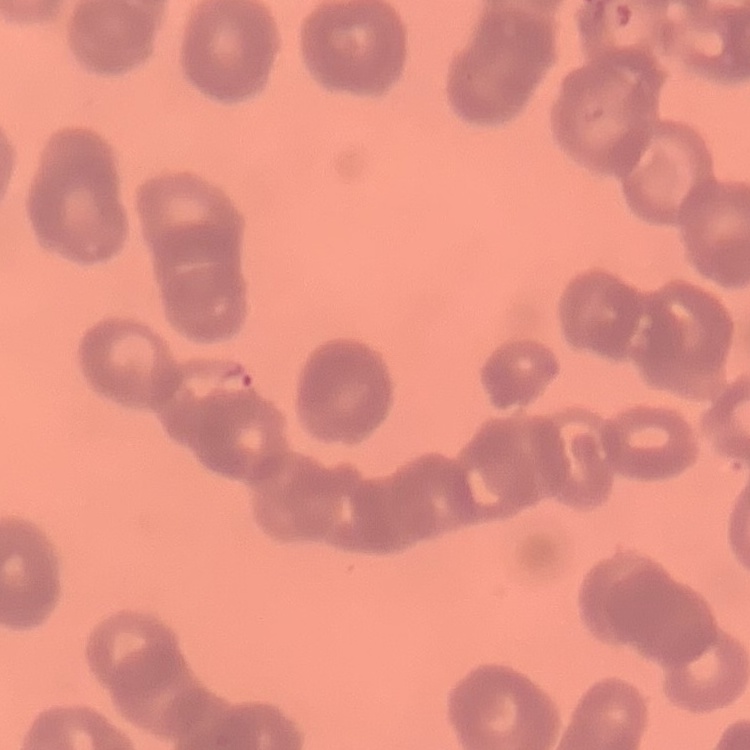

The erythrocytes exhibit rouleaux formation. Field's or Giemsa stain. Thin blood smear. One tile cut from a larger photomicrograph.